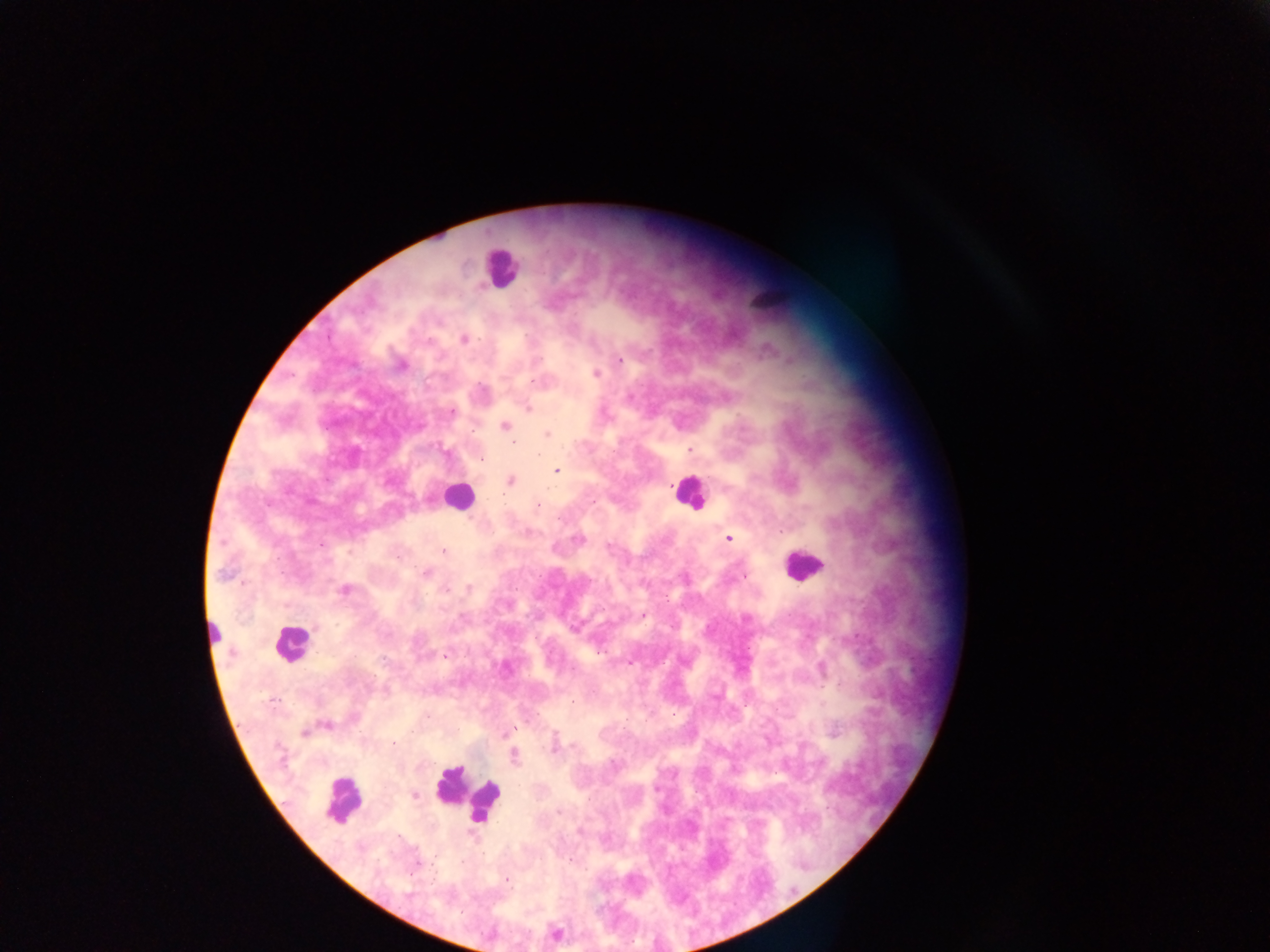

Approximate centers as {x, y} in pixels. Leukocyte locations: {501, 268}, {769, 295}, {688, 493}, {457, 495}, {802, 564}, {213, 635}, {290, 643}, {465, 796}, {343, 799}. Plasmodium parasite locations: {464, 339}, {619, 359}, {402, 365}, {596, 374}, {535, 382}, {528, 408}, {451, 413}, {504, 426}, {546, 434}, {514, 442}, {689, 450}, {539, 456}, {483, 460}, {557, 470}, {511, 481}, {594, 502}, {537, 505}, {559, 520}, {728, 538}, {443, 551}, {426, 573}, {224, 574}, {744, 576}, {469, 588}, {346, 590}, {446, 590}, {643, 615}, {574, 629}, {599, 652}, {231, 653}, {445, 657}, {630, 663}, {427, 716}, {327, 725}, {513, 728}, {304, 732}, {393, 743}, {554, 746}, {574, 746}, {514, 756}, {414, 795}, {558, 811}, {569, 859}, {462, 863}, {506, 880}. Thick blood film. Collected in Ghana. Single field of view. Mobile-phone photograph taken through the microscope. Image is 1270×952 pixels.